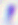

Summary:
  - Modality: micrograph
  - Identification: Toxoplasma gondii
  - Magnification: 400x